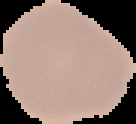 Image is 136×124 pixels. The area outside the segmented cell region is set to black. From a thin blood smear. Result: no Plasmodium parasites detected.